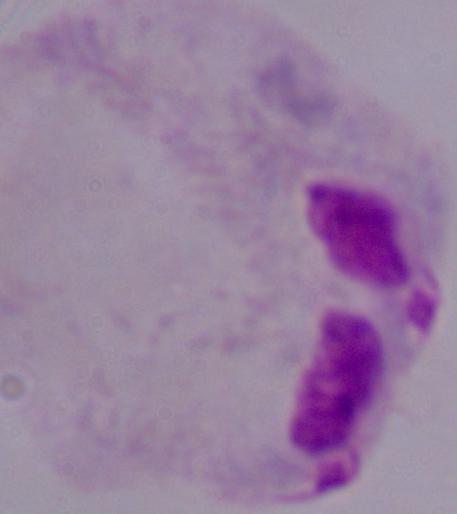

Summary:
  - Identification: trichomonad
  - Magnification: 1000x
  - Modality: micrograph